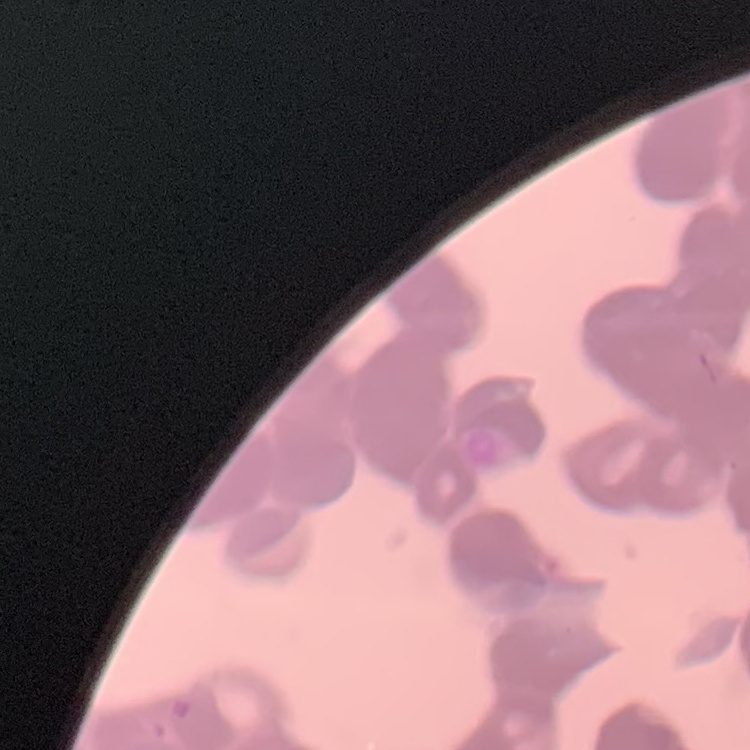
Summary:
  - Erythrocyte morphology: rouleaux formation
  - Stain: Field's or Giemsa
  - Preparation: thin peripheral smear
  - Image type: square crop of a larger photomicrograph